Locate and identify every blood parasite.
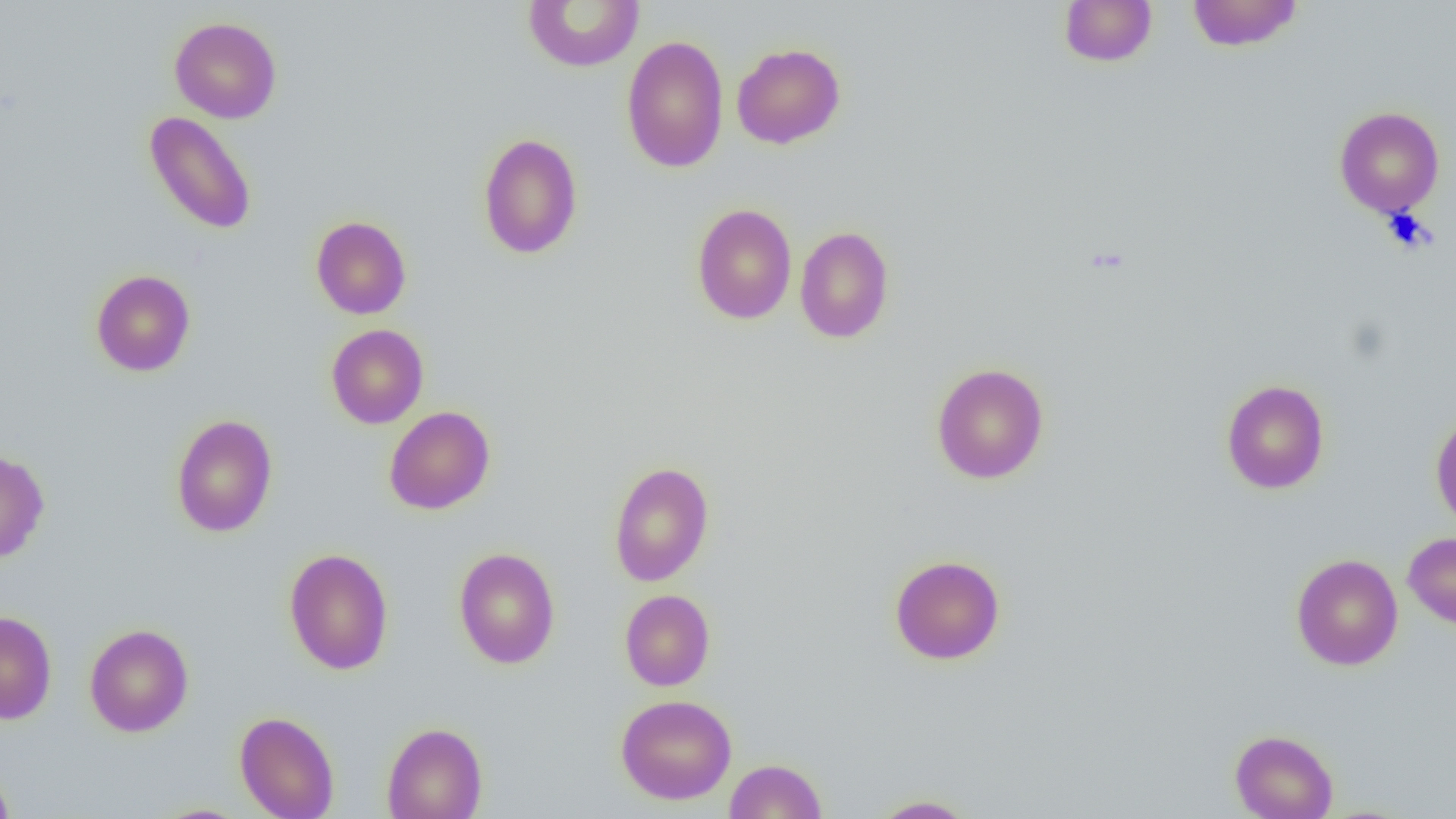
No blood parasites observed.

Approximate bounding boxes as named x1/y1/x2/y2 corners in pixels. Uninfected red blood cell locations: (x1=522, y1=0, x2=645, y2=72), (x1=1058, y1=0, x2=1157, y2=67), (x1=1186, y1=0, x2=1304, y2=52), (x1=169, y1=17, x2=282, y2=123), (x1=621, y1=34, x2=729, y2=173), (x1=732, y1=43, x2=846, y2=149), (x1=1333, y1=106, x2=1445, y2=218), (x1=144, y1=111, x2=257, y2=235), (x1=478, y1=132, x2=583, y2=259), (x1=692, y1=204, x2=797, y2=325), (x1=311, y1=215, x2=411, y2=319), (x1=794, y1=226, x2=895, y2=343), (x1=91, y1=270, x2=195, y2=377), (x1=326, y1=324, x2=428, y2=429), (x1=931, y1=363, x2=1049, y2=484), (x1=1221, y1=379, x2=1330, y2=494), (x1=384, y1=406, x2=495, y2=515), (x1=1430, y1=409, x2=1456, y2=531), (x1=171, y1=414, x2=278, y2=537), (x1=0, y1=449, x2=49, y2=563), (x1=608, y1=461, x2=714, y2=587), (x1=1403, y1=531, x2=1456, y2=631), (x1=283, y1=547, x2=394, y2=675), (x1=453, y1=547, x2=560, y2=669), (x1=1290, y1=553, x2=1403, y2=670), (x1=889, y1=554, x2=1006, y2=665), (x1=619, y1=589, x2=715, y2=691), (x1=0, y1=610, x2=57, y2=724), (x1=84, y1=623, x2=193, y2=737), (x1=616, y1=694, x2=737, y2=805), (x1=234, y1=711, x2=339, y2=819), (x1=381, y1=722, x2=488, y2=819), (x1=1229, y1=729, x2=1338, y2=819), (x1=724, y1=758, x2=827, y2=818), (x1=0, y1=763, x2=16, y2=819), (x1=870, y1=795, x2=977, y2=818). Slide-level diagnosis: no evidence of blood parasites. Captured at 1000x magnification. Thin blood film. Single field of view. Image is 1456×819 pixels. Light microscopy.